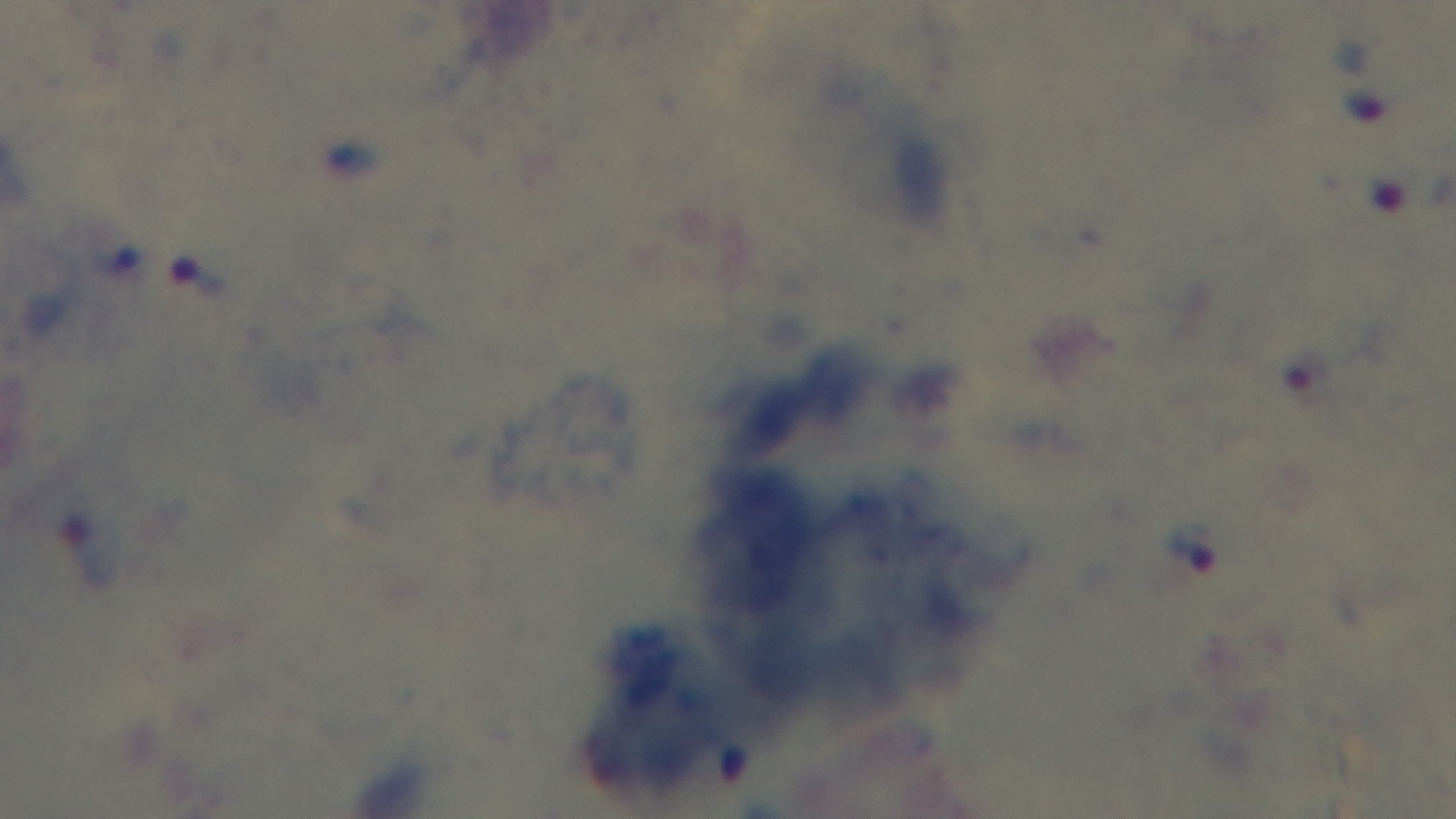

{
  "objective": "100x oil immersion",
  "capture": "mounted 4K digital camera",
  "malaria_status": "positive",
  "field_of_view": "one from the slide",
  "preparation": "thick blood film",
  "modality": "light microscopy",
  "stain": "Giemsa"
}